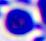
Photomicrograph. A leukocyte is shown. Captured at 400x magnification.